Assess this cell for malaria.
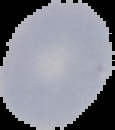
Uninfected.

Summary:
  - Preparation: thin blood smear
  - Image type: segmented cell region on a black background
  - Image size: 115×130 pixels